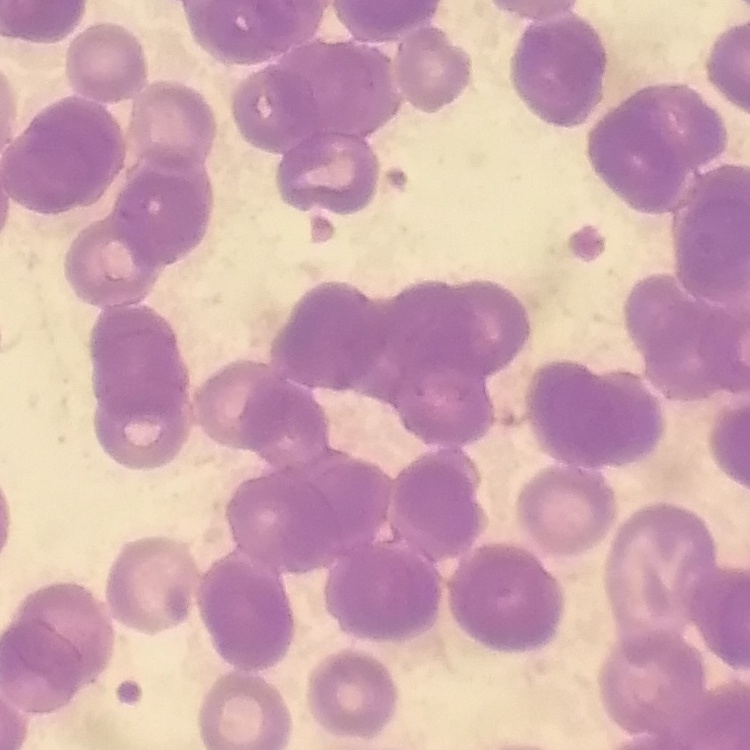
erythrocyte morphology = rouleaux formation
preparation = thin peripheral smear
stain = Field's or Giemsa
image type = one tile cut from a larger photomicrograph